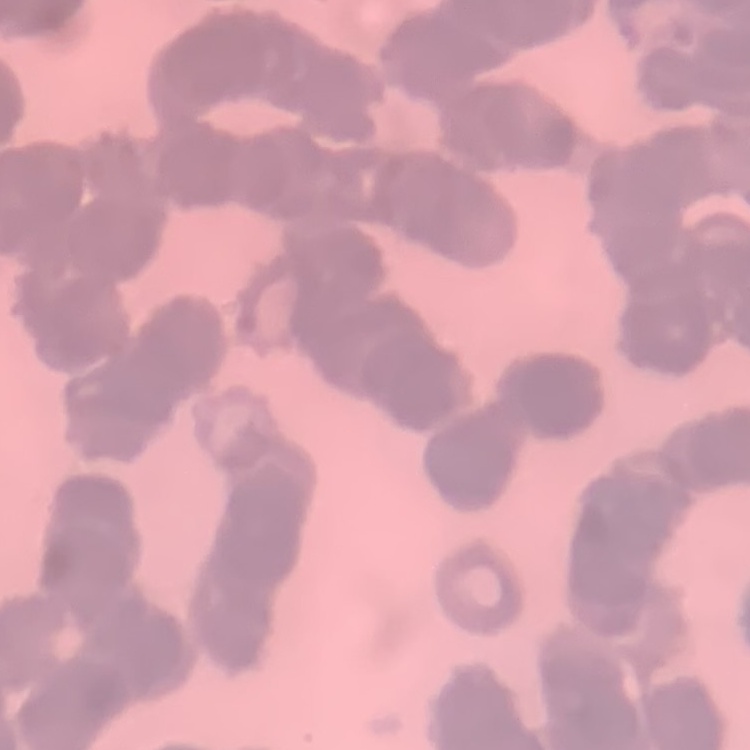
The red blood cells show rouleaux formation. One tile cut from a larger photomicrograph. Field's or Giemsa stain. Thin blood film.